Locate every Plasmodium parasite.
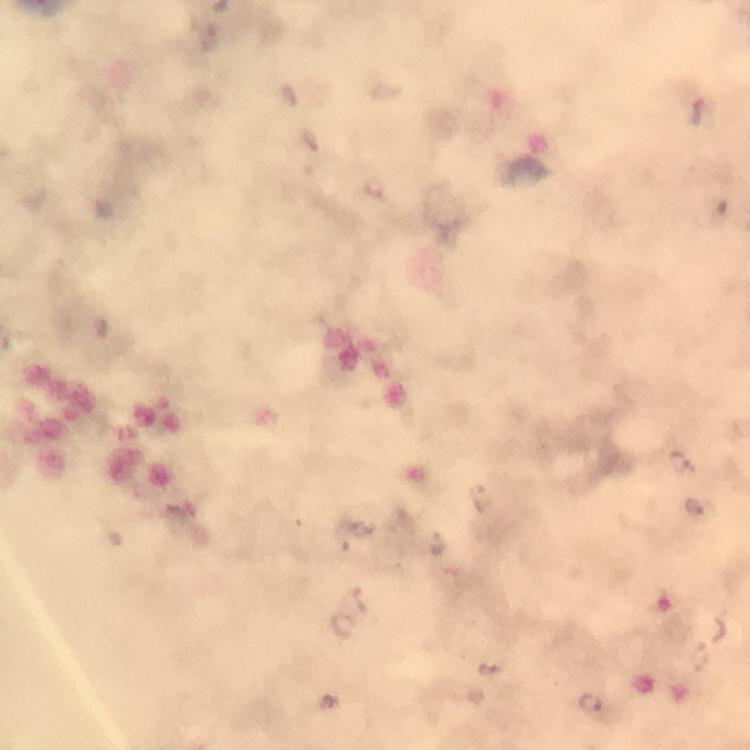

Approximate centers as {x, y} in pixels.
Plasmodium parasites: {699, 110}, {374, 189}, {682, 461}, {481, 497}, {696, 508}, {437, 545}, {344, 625}, {491, 671}, {592, 704}.

Summary:
  - Stain: Giemsa
  - Magnification: 100x
  - Image size: 750×750 pixels
  - Preparation: thick smear
  - Capture: smartphone photograph through a microscope
  - Cropped from: a single field of view
  - Immersion oil: used
  - Context: from a malaria diagnostic workup